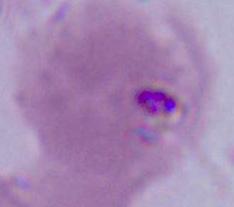

Captured at 1000x magnification. Micrograph. A red blood cell is shown.